Report the malaria status of this cell.
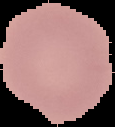
Uninfected.

Summary:
  - Image type: segmented cell region on a black background
  - Preparation: thin blood smear
  - Image size: 115×127 pixels